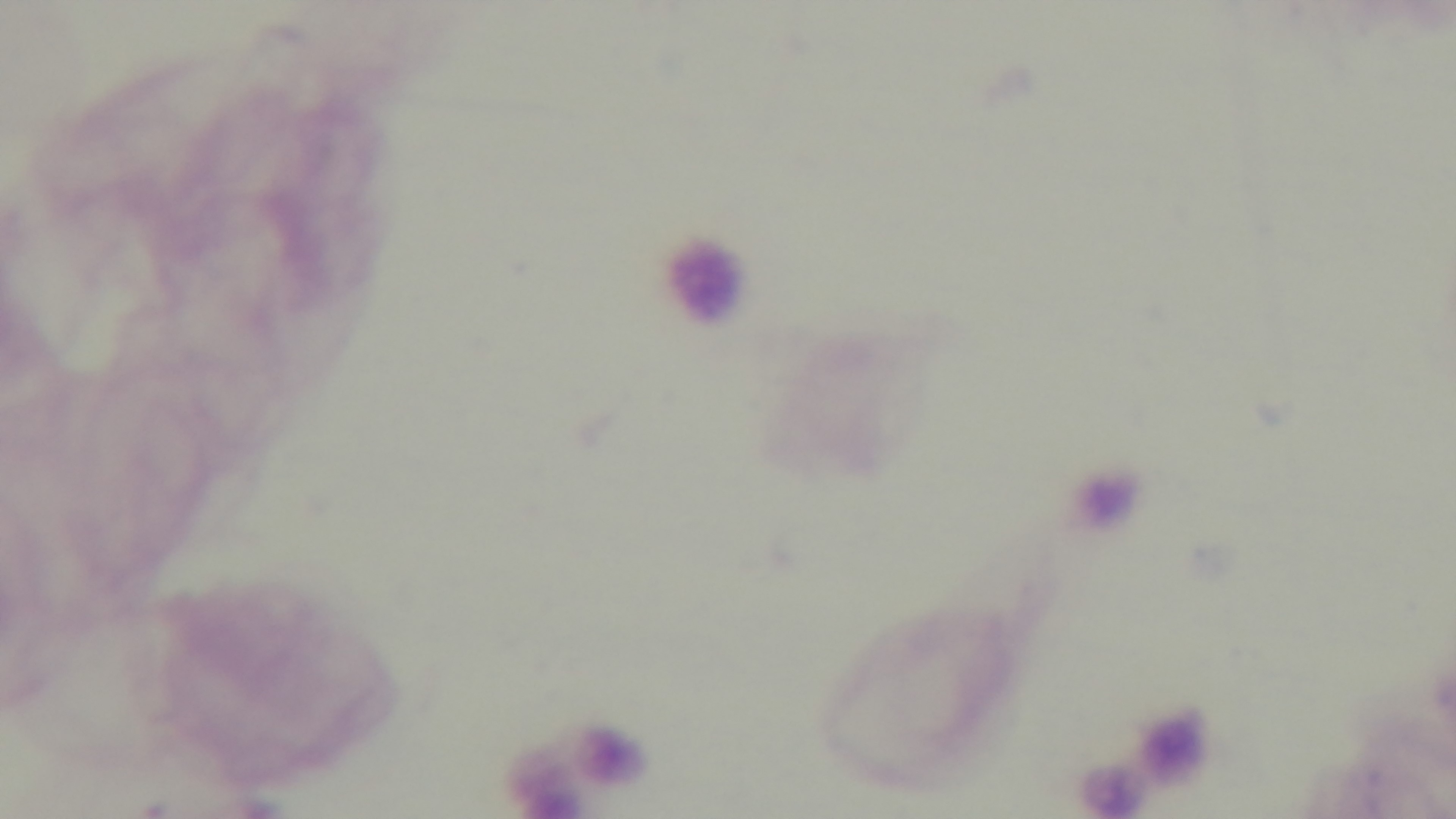

100x oil-immersion objective. Light microscopy. Mounted 4K digital camera. Preparation: thick smear. One field from the slide. Giemsa-stained. Malaria status: uninfected.